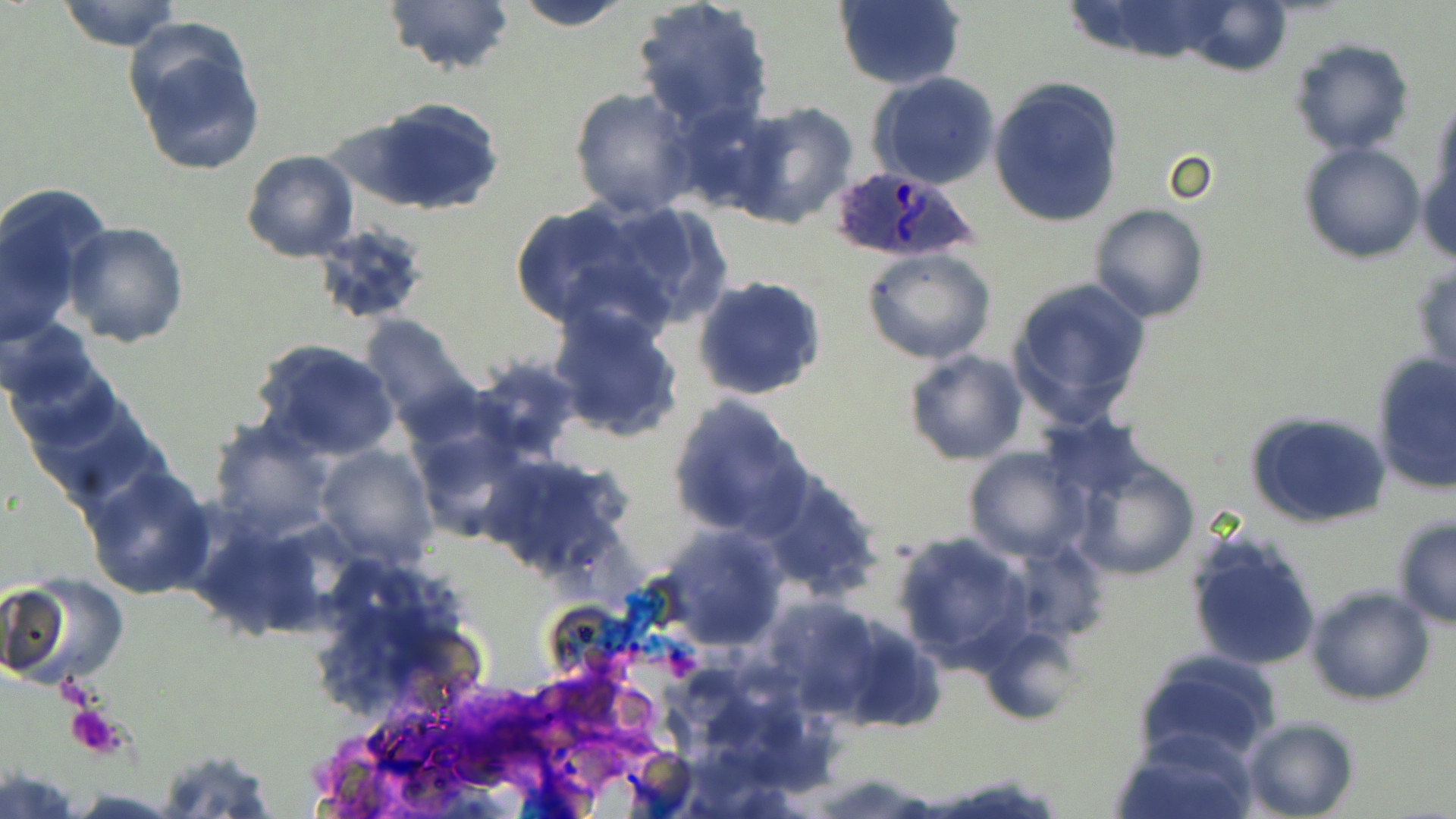
Summary:
  - Coordinate format: approximate bounding boxes as [x1, y1, x2, y2] in pixels
  - Platelet locations: [65, 704, 123, 758]
  - Uninfected red blood cell locations: [57, 0, 182, 52], [383, 0, 517, 78], [509, 0, 636, 31], [631, 0, 774, 135], [833, 0, 966, 91], [1060, 0, 1243, 65], [1172, 0, 1294, 75], [127, 23, 267, 176], [1290, 38, 1414, 156], [870, 73, 1001, 191], [988, 78, 1125, 228], [568, 87, 700, 218], [352, 97, 507, 216], [725, 101, 857, 229], [1417, 124, 1456, 273], [1300, 143, 1424, 263], [240, 150, 359, 261], [0, 184, 105, 339], [506, 197, 671, 337], [587, 198, 733, 331], [1088, 203, 1209, 322], [62, 221, 189, 347], [309, 223, 433, 325], [863, 248, 995, 364], [1411, 257, 1456, 378], [693, 275, 826, 402], [1008, 278, 1150, 423], [547, 305, 685, 443], [358, 313, 481, 438], [4, 324, 118, 448], [250, 336, 403, 463], [903, 350, 1028, 465], [1371, 353, 1456, 493], [463, 358, 587, 462], [25, 389, 167, 512], [667, 395, 812, 540], [1246, 411, 1391, 528], [205, 418, 338, 540], [314, 445, 439, 566], [961, 447, 1091, 563], [478, 451, 635, 584], [1068, 457, 1201, 582], [81, 464, 215, 600], [755, 471, 886, 602], [1390, 515, 1456, 632], [644, 525, 788, 655], [892, 531, 1035, 674], [1185, 531, 1322, 672], [4, 576, 129, 687], [1306, 586, 1435, 706], [980, 624, 1084, 721], [1132, 650, 1284, 768], [1241, 716, 1357, 819], [1112, 728, 1258, 818], [157, 747, 277, 817], [0, 768, 79, 816], [67, 789, 185, 817]
  - Plasmodium ovale-infected red blood cell locations: [827, 165, 979, 264]
  - Slide-level diagnosis: Plasmodium ovale
  - Field of view: one of a larger specimen
  - Magnification: 1000x
  - Preparation: thin blood smear
  - Modality: optical microscopy
  - Image size: 1456×819 pixels
  - Stain: May-Grünwald-Giemsa